Outline every malaria parasite, every leukocyte, and every artifact (stain precipitate or debris).
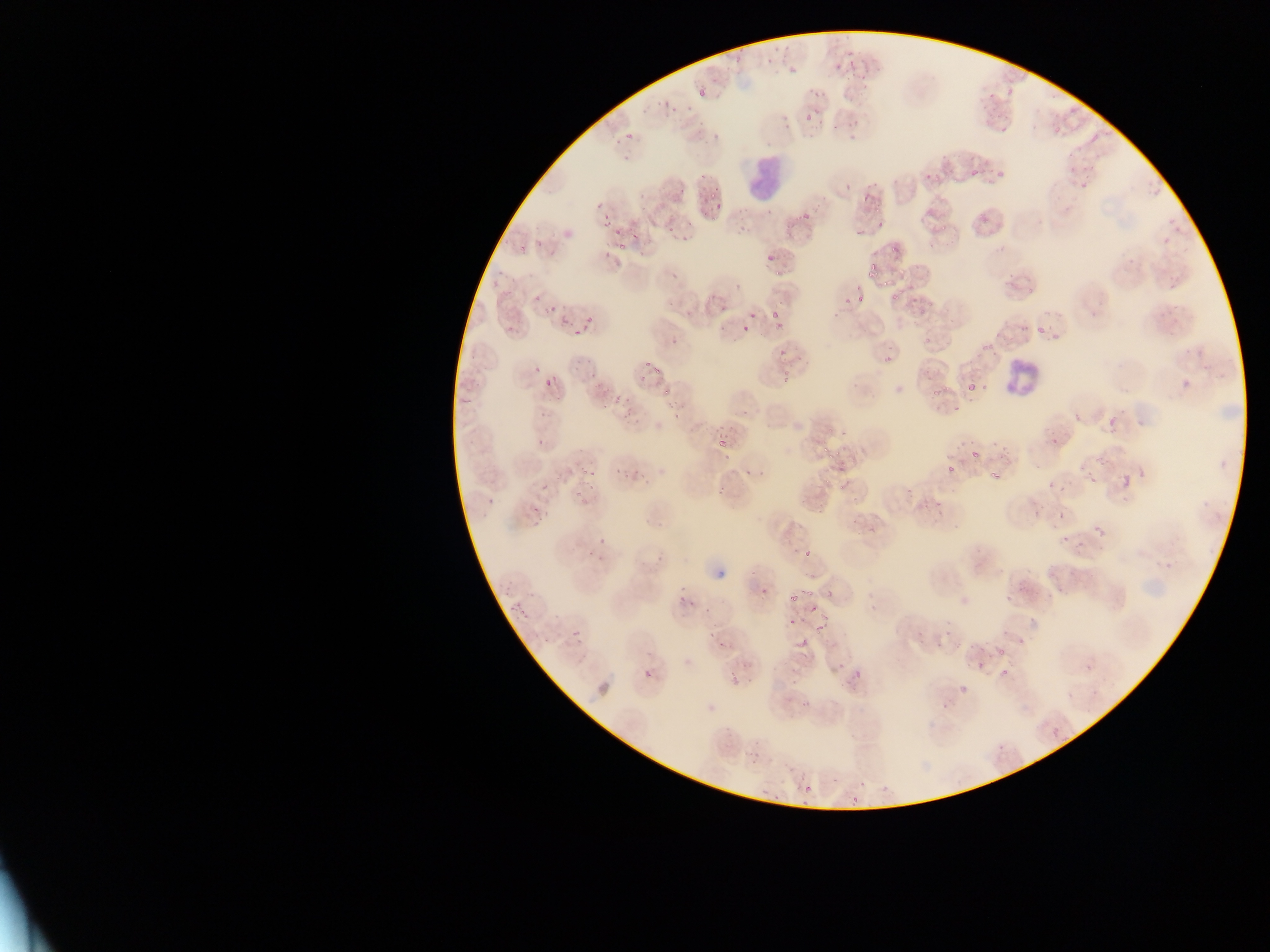

Approximate bounding boxes as {left, top, right, bottom} in pixels.
Malaria parasites: {749, 37, 777, 64}, {829, 44, 862, 68}, {780, 62, 790, 75}, {849, 67, 870, 87}, {984, 74, 1008, 100}, {689, 84, 712, 101}, {659, 89, 680, 117}, {793, 103, 813, 127}, {983, 105, 1012, 135}, {1047, 116, 1069, 136}, {626, 132, 633, 141}, {1091, 133, 1099, 141}, {1056, 147, 1084, 179}, {920, 150, 948, 178}, {971, 169, 980, 177}, {854, 177, 880, 201}, {659, 180, 681, 195}, {695, 192, 725, 213}, {855, 201, 886, 232}, {918, 201, 943, 215}, {802, 212, 810, 220}, {658, 214, 680, 237}, {601, 216, 616, 230}, {618, 225, 642, 252}, {550, 228, 576, 241}, {763, 243, 790, 263}, {863, 251, 889, 281}, {664, 258, 686, 287}, {998, 264, 1029, 299}, {490, 280, 509, 297}, {887, 280, 913, 304}, {838, 282, 866, 306}, {698, 287, 734, 318}, {520, 292, 540, 311}, {532, 306, 547, 325}, {765, 307, 791, 334}, {552, 310, 572, 332}, {571, 320, 597, 336}, {1007, 322, 1025, 339}, {1031, 322, 1065, 342}, {735, 326, 747, 340}, {663, 338, 680, 358}, {877, 341, 912, 369}, {773, 347, 794, 367}, {570, 352, 591, 376}, {642, 354, 670, 379}, {781, 368, 805, 385}, {533, 370, 563, 397}, {926, 372, 954, 399}, {583, 373, 600, 397}, {967, 383, 975, 391}, {607, 389, 632, 411}, {1072, 396, 1087, 428}, {711, 406, 751, 451}, {1105, 410, 1125, 432}, {1045, 419, 1064, 443}, {533, 426, 551, 450}, {819, 432, 843, 455}, {967, 440, 986, 460}, {829, 446, 853, 476}, {934, 449, 956, 482}, {562, 454, 582, 474}, {987, 456, 1008, 484}, {624, 460, 642, 479}, {577, 465, 600, 497}, {715, 465, 736, 493}, {1087, 474, 1097, 482}, {1122, 475, 1131, 487}, {837, 480, 854, 497}, {1048, 481, 1055, 490}, {480, 491, 496, 521}, {529, 498, 553, 524}, {1053, 502, 1070, 522}, {1090, 506, 1118, 537}, {1056, 528, 1070, 545}, {590, 539, 619, 560}, {803, 548, 812, 557}, {1020, 572, 1036, 591}, {757, 585, 769, 601}, {781, 585, 808, 607}, {674, 588, 695, 619}, {509, 601, 528, 620}, {814, 603, 833, 630}, {785, 615, 802, 624}, {571, 628, 581, 639}, {928, 628, 953, 657}, {976, 631, 995, 662}, {707, 635, 726, 653}, {798, 636, 810, 647}, {641, 649, 661, 688}, {991, 650, 1013, 681}, {737, 659, 748, 680}, {1083, 662, 1093, 673}, {844, 663, 872, 683}, {955, 679, 968, 690}, {1067, 691, 1075, 700}, {800, 694, 817, 711}, {1052, 728, 1061, 737}, {747, 744, 770, 768}, {803, 785, 812, 795}, {852, 795, 860, 803} | approximate {x, y} pixel centers of objects too small to bound: {852, 137}.
Leukocytes: {747, 160, 805, 203}, {994, 354, 1030, 400}.

country = Ghana
capture = mobile-phone photograph through a microscope
preparation = thin blood smear
image size = 1270×952 pixels
field of view = single